State which parasite is depicted.
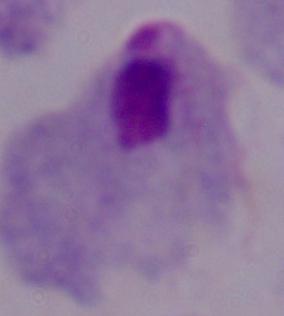
This is a trichomonad.

modality: micrograph
magnification: 1000x